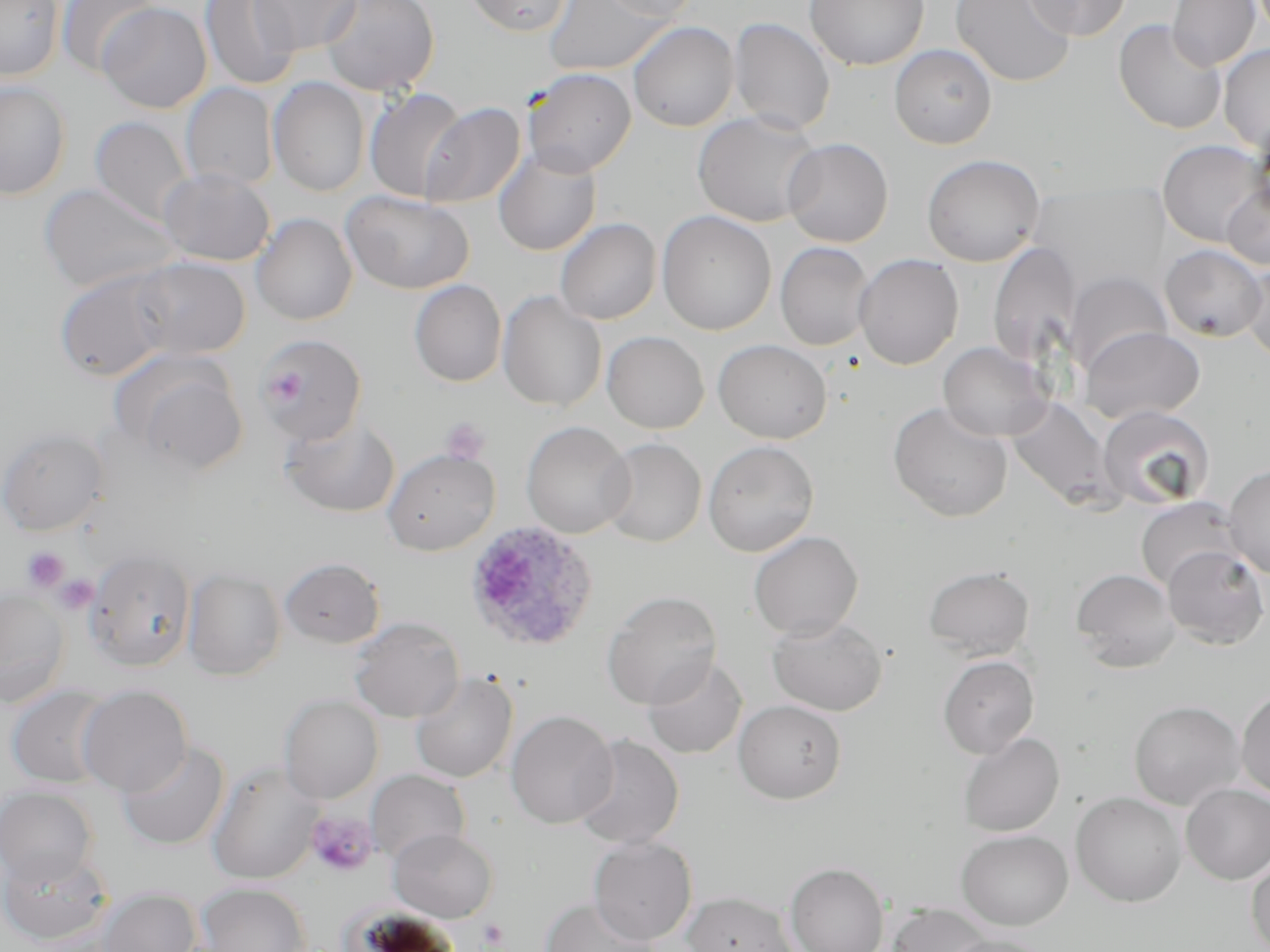
Summary:
  - Coordinate format: approximate bounding boxes as named x1/y1/x2/y2 corners in pixels
  - Plasmodium ovale-infected red blood cell locations: (x1=462, y1=520, x2=600, y2=654)
  - Uninfected red blood cell locations: (x1=0, y1=0, x2=65, y2=82), (x1=58, y1=0, x2=162, y2=78), (x1=200, y1=0, x2=302, y2=91), (x1=251, y1=0, x2=361, y2=55), (x1=320, y1=0, x2=440, y2=97), (x1=464, y1=0, x2=572, y2=36), (x1=543, y1=0, x2=668, y2=76), (x1=600, y1=0, x2=703, y2=22), (x1=950, y1=0, x2=1076, y2=88), (x1=1024, y1=0, x2=1130, y2=40), (x1=1167, y1=0, x2=1260, y2=71), (x1=805, y1=1, x2=929, y2=70), (x1=98, y1=2, x2=212, y2=114), (x1=728, y1=18, x2=835, y2=134), (x1=1114, y1=19, x2=1226, y2=134), (x1=628, y1=21, x2=739, y2=132), (x1=889, y1=44, x2=997, y2=149), (x1=1218, y1=44, x2=1270, y2=153), (x1=523, y1=68, x2=636, y2=176), (x1=268, y1=77, x2=371, y2=196), (x1=1, y1=80, x2=72, y2=199), (x1=180, y1=83, x2=277, y2=191), (x1=364, y1=87, x2=468, y2=202), (x1=420, y1=101, x2=526, y2=209), (x1=693, y1=110, x2=822, y2=227), (x1=89, y1=116, x2=193, y2=226), (x1=782, y1=137, x2=893, y2=247), (x1=1157, y1=139, x2=1269, y2=247), (x1=493, y1=146, x2=602, y2=256), (x1=922, y1=154, x2=1045, y2=267), (x1=158, y1=168, x2=275, y2=266), (x1=1221, y1=182, x2=1270, y2=271), (x1=39, y1=183, x2=179, y2=294), (x1=341, y1=189, x2=474, y2=294), (x1=657, y1=210, x2=776, y2=336), (x1=251, y1=213, x2=357, y2=325), (x1=555, y1=218, x2=661, y2=325), (x1=988, y1=241, x2=1082, y2=368), (x1=775, y1=242, x2=874, y2=351), (x1=1159, y1=244, x2=1268, y2=341), (x1=853, y1=254, x2=963, y2=369), (x1=131, y1=257, x2=250, y2=359), (x1=1240, y1=263, x2=1270, y2=364), (x1=53, y1=268, x2=180, y2=382), (x1=1064, y1=271, x2=1173, y2=377), (x1=409, y1=279, x2=507, y2=387), (x1=498, y1=292, x2=607, y2=412), (x1=1079, y1=326, x2=1206, y2=425), (x1=602, y1=331, x2=709, y2=433), (x1=256, y1=333, x2=367, y2=445), (x1=713, y1=339, x2=832, y2=444), (x1=938, y1=341, x2=1054, y2=441), (x1=113, y1=351, x2=248, y2=475), (x1=1006, y1=397, x2=1120, y2=510), (x1=887, y1=401, x2=1013, y2=522), (x1=1097, y1=404, x2=1215, y2=511), (x1=281, y1=416, x2=400, y2=518), (x1=521, y1=421, x2=634, y2=538), (x1=0, y1=426, x2=109, y2=536), (x1=599, y1=438, x2=706, y2=547), (x1=703, y1=440, x2=819, y2=556), (x1=382, y1=448, x2=500, y2=555), (x1=1223, y1=464, x2=1270, y2=579), (x1=1135, y1=496, x2=1243, y2=592), (x1=748, y1=530, x2=864, y2=640), (x1=1162, y1=546, x2=1269, y2=650), (x1=85, y1=549, x2=197, y2=671), (x1=278, y1=557, x2=386, y2=649), (x1=922, y1=565, x2=1035, y2=661), (x1=183, y1=567, x2=286, y2=681), (x1=1070, y1=568, x2=1181, y2=672), (x1=0, y1=587, x2=70, y2=707), (x1=601, y1=590, x2=723, y2=709), (x1=767, y1=614, x2=888, y2=716), (x1=348, y1=617, x2=465, y2=723), (x1=938, y1=655, x2=1039, y2=759), (x1=642, y1=656, x2=747, y2=759), (x1=410, y1=671, x2=518, y2=783), (x1=6, y1=685, x2=115, y2=788), (x1=76, y1=685, x2=193, y2=796), (x1=1236, y1=688, x2=1270, y2=800), (x1=279, y1=694, x2=383, y2=804), (x1=733, y1=699, x2=846, y2=803), (x1=1129, y1=700, x2=1245, y2=809), (x1=505, y1=710, x2=618, y2=829), (x1=958, y1=731, x2=1065, y2=837), (x1=572, y1=735, x2=684, y2=850), (x1=117, y1=741, x2=230, y2=851), (x1=207, y1=760, x2=322, y2=885), (x1=366, y1=769, x2=471, y2=866), (x1=1181, y1=783, x2=1270, y2=885), (x1=0, y1=786, x2=99, y2=886), (x1=1071, y1=792, x2=1186, y2=908), (x1=388, y1=828, x2=498, y2=922), (x1=956, y1=829, x2=1073, y2=930), (x1=588, y1=837, x2=698, y2=944), (x1=0, y1=849, x2=112, y2=945), (x1=1246, y1=852, x2=1270, y2=952), (x1=785, y1=862, x2=889, y2=952), (x1=196, y1=883, x2=311, y2=952), (x1=96, y1=887, x2=201, y2=952), (x1=681, y1=891, x2=798, y2=952), (x1=540, y1=897, x2=662, y2=952), (x1=887, y1=904, x2=995, y2=952), (x1=944, y1=934, x2=1050, y2=952)
  - Platelet locations: (x1=441, y1=417, x2=491, y2=465), (x1=22, y1=546, x2=71, y2=592), (x1=54, y1=574, x2=99, y2=614), (x1=305, y1=810, x2=379, y2=878), (x1=477, y1=918, x2=510, y2=950)
  - Slide-level diagnosis: Plasmodium ovale
  - Image size: 1270×952 pixels
  - Stain: May-Grünwald-Giemsa
  - Modality: optical microscopy
  - Magnification: 1000x
  - Preparation: thin blood film
  - Field of view: single